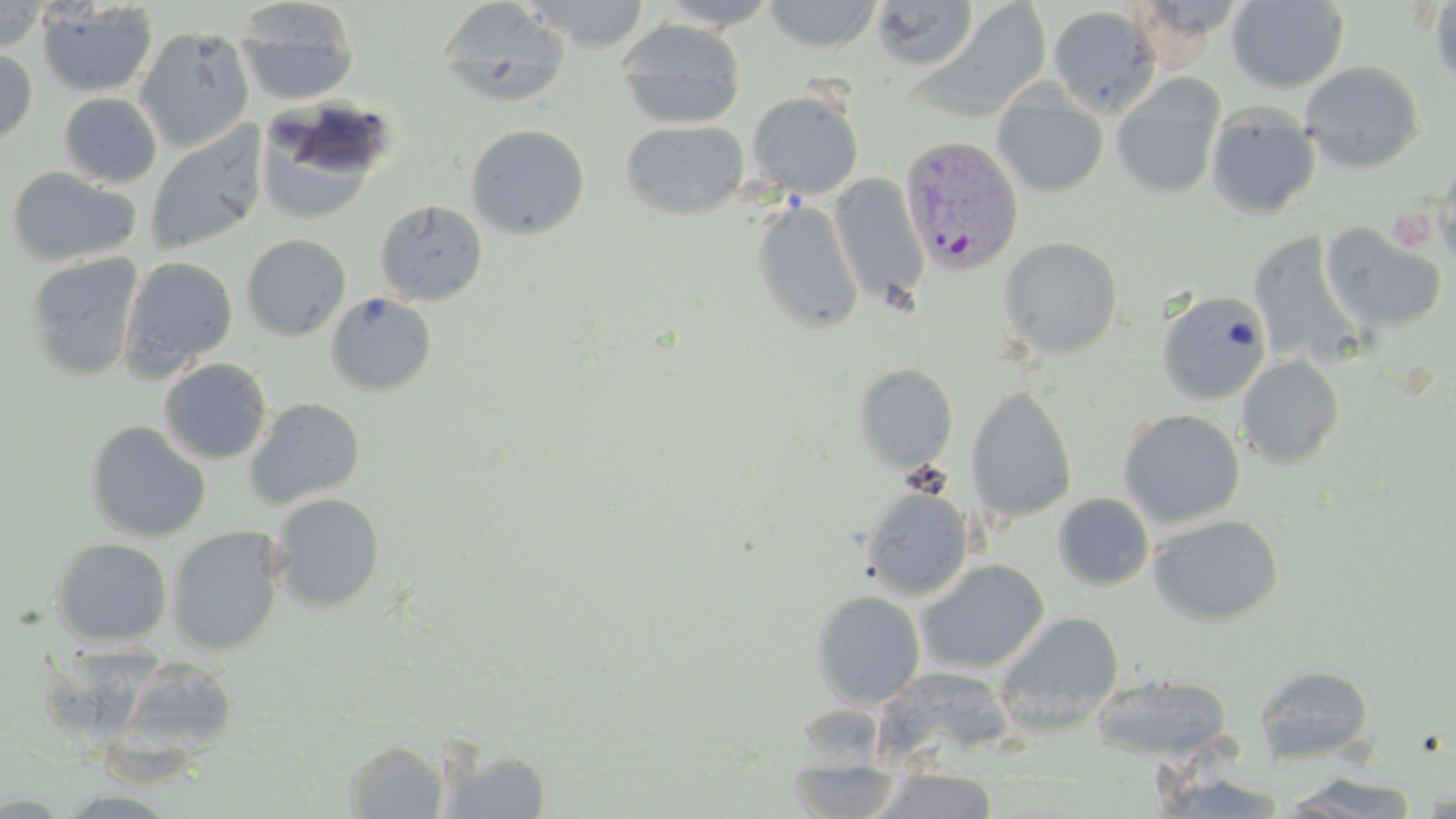
Summary:
  - Coordinate format: approximate bounding boxes as (x1, y1, x2, y2) in pixels
  - Plasmodium vivax-infected red blood cell locations: (898, 135, 1024, 273)
  - Uninfected red blood cell locations: (519, 0, 653, 52), (657, 0, 781, 30), (763, 0, 883, 53), (1226, 0, 1349, 93), (1428, 0, 1456, 90), (0, 1, 50, 52), (235, 1, 360, 107), (436, 1, 572, 108), (868, 1, 979, 72), (36, 2, 158, 98), (912, 4, 1053, 122), (1047, 5, 1161, 116), (616, 20, 746, 130), (135, 26, 255, 152), (0, 47, 38, 147), (1300, 61, 1425, 173), (1111, 72, 1227, 201), (747, 91, 864, 200), (992, 91, 1108, 198), (58, 92, 162, 188), (255, 99, 395, 220), (1205, 102, 1322, 219), (620, 120, 749, 220), (144, 123, 268, 256), (465, 124, 590, 240), (1435, 153, 1456, 273), (6, 166, 140, 266), (830, 174, 930, 308), (750, 197, 865, 335), (374, 199, 488, 306), (1320, 222, 1448, 333), (1247, 232, 1363, 367), (241, 234, 352, 341), (998, 236, 1124, 358), (24, 253, 144, 382), (119, 256, 239, 377), (1156, 289, 1273, 405), (325, 292, 437, 396), (1235, 356, 1345, 469), (159, 358, 272, 465), (853, 363, 958, 472), (966, 386, 1078, 523), (245, 398, 366, 508), (1118, 408, 1245, 528), (85, 420, 210, 542), (861, 487, 973, 599), (270, 493, 387, 612), (1053, 493, 1154, 590), (1148, 513, 1285, 626), (167, 526, 285, 655), (50, 538, 172, 648), (915, 559, 1050, 674), (810, 589, 926, 709), (996, 612, 1125, 707), (113, 655, 240, 760), (1253, 663, 1376, 766), (1089, 675, 1233, 762), (343, 739, 450, 818), (439, 746, 553, 818), (787, 768, 907, 818), (874, 772, 1000, 817), (1280, 772, 1423, 818)
  - Slide-level diagnosis: Plasmodium vivax
  - Field of view: single
  - Image size: 1456×819 pixels
  - Magnification: 1000x
  - Stain: May-Grünwald-Giemsa
  - Modality: light microscopy
  - Preparation: thin blood film